Classify this cell by malaria status.
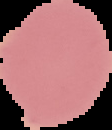

Uninfected.

image type = segmented cell region on a black background
preparation = thin blood film
image size = 112×130 pixels